Assess this cell for malaria.
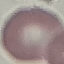
It is uninfected.

Summary:
  - Image type: cell patch, automatically extracted from a larger field of view and resized to 64 × 64 pixels
  - Stain: Giemsa
  - Capture: smartphone camera at the microscope eyepiece
  - Preparation: thin smear